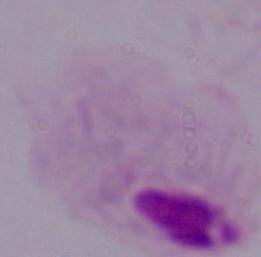
A trichomonad is shown. Captured at 1000x magnification. Micrograph.